Name the parasite shown.
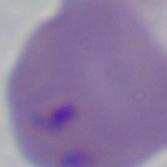

This is Babesia.

Summary:
  - Magnification: 1000x
  - Modality: photomicrograph